Locate every blood parasite and identify its species.
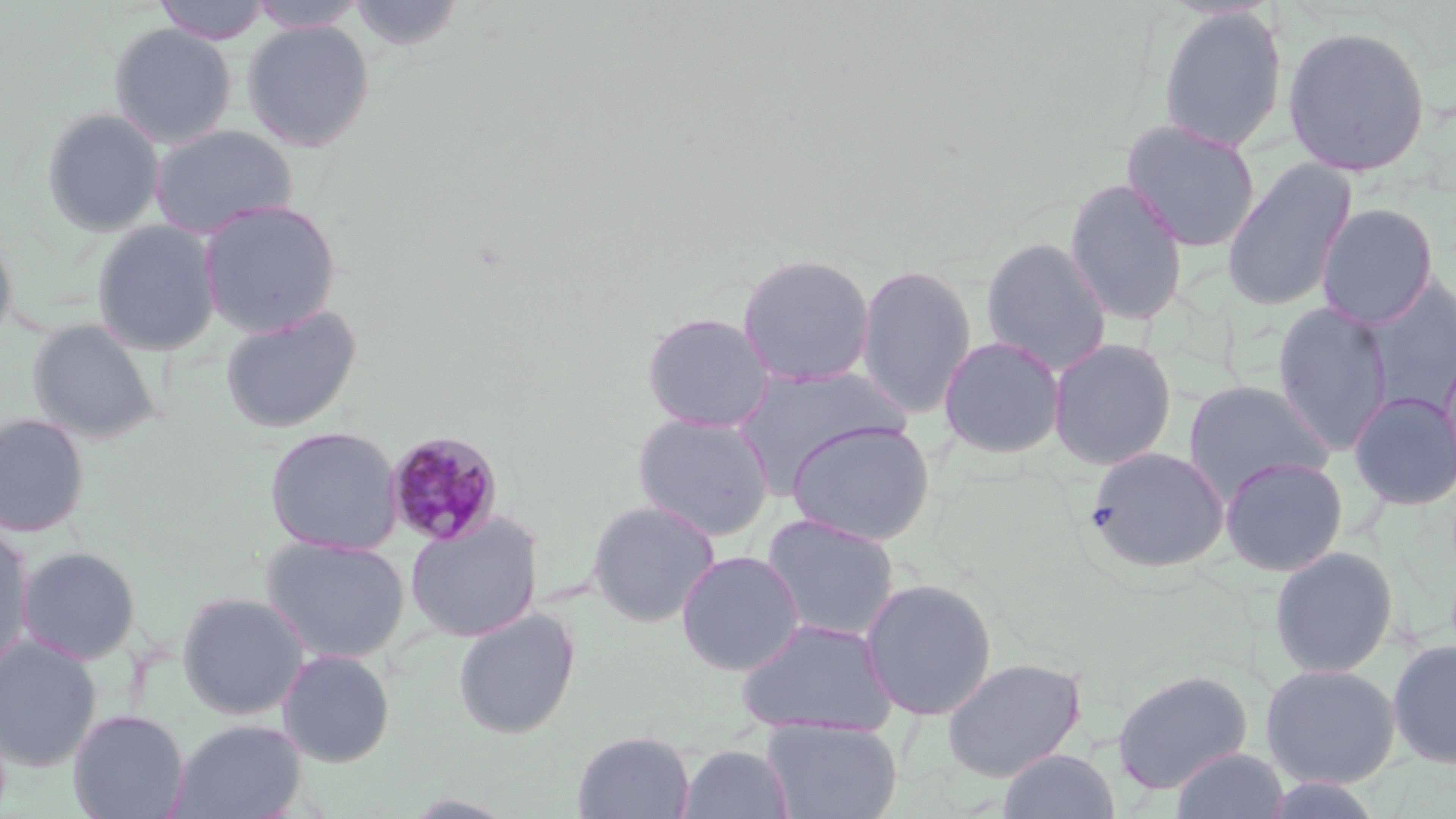
Approximate bounding boxes as named x1/y1/x2/y2 corners in pixels.
Plasmodium malariae-infected red blood cells: (x1=384, y1=431, x2=504, y2=546).
No Plasmodium falciparum, Plasmodium ovale, Plasmodium vivax, Babesia divergens, or Trypanosoma brucei observed.

Uninfected red blood cell locations: (x1=154, y1=0, x2=272, y2=43), (x1=246, y1=0, x2=368, y2=33), (x1=346, y1=0, x2=467, y2=52), (x1=1157, y1=5, x2=1289, y2=154), (x1=242, y1=19, x2=376, y2=152), (x1=108, y1=23, x2=237, y2=148), (x1=1281, y1=24, x2=1432, y2=178), (x1=41, y1=107, x2=164, y2=236), (x1=1121, y1=119, x2=1261, y2=252), (x1=150, y1=124, x2=299, y2=238), (x1=1221, y1=158, x2=1357, y2=313), (x1=1063, y1=177, x2=1189, y2=326), (x1=198, y1=199, x2=342, y2=338), (x1=1316, y1=203, x2=1439, y2=329), (x1=91, y1=220, x2=222, y2=356), (x1=0, y1=228, x2=17, y2=347), (x1=980, y1=237, x2=1112, y2=374), (x1=736, y1=252, x2=876, y2=387), (x1=855, y1=263, x2=977, y2=418), (x1=1360, y1=274, x2=1456, y2=417), (x1=1271, y1=301, x2=1393, y2=455), (x1=219, y1=303, x2=362, y2=435), (x1=641, y1=311, x2=776, y2=433), (x1=26, y1=318, x2=163, y2=444), (x1=938, y1=336, x2=1066, y2=458), (x1=1047, y1=337, x2=1178, y2=470), (x1=1437, y1=344, x2=1456, y2=497), (x1=729, y1=366, x2=910, y2=494), (x1=1182, y1=380, x2=1334, y2=500), (x1=1349, y1=390, x2=1456, y2=511), (x1=633, y1=412, x2=775, y2=542), (x1=0, y1=413, x2=90, y2=537), (x1=786, y1=419, x2=935, y2=546), (x1=263, y1=426, x2=404, y2=555), (x1=1085, y1=447, x2=1230, y2=574), (x1=1219, y1=456, x2=1348, y2=576), (x1=586, y1=499, x2=721, y2=628), (x1=404, y1=513, x2=544, y2=642), (x1=761, y1=513, x2=900, y2=642), (x1=0, y1=522, x2=34, y2=673), (x1=261, y1=536, x2=410, y2=664), (x1=16, y1=546, x2=141, y2=665), (x1=1269, y1=546, x2=1399, y2=678), (x1=675, y1=549, x2=805, y2=676), (x1=859, y1=578, x2=998, y2=720), (x1=177, y1=591, x2=310, y2=720), (x1=452, y1=608, x2=581, y2=739), (x1=735, y1=617, x2=897, y2=736), (x1=0, y1=635, x2=102, y2=772), (x1=1387, y1=639, x2=1456, y2=769), (x1=278, y1=649, x2=395, y2=767), (x1=941, y1=657, x2=1086, y2=781), (x1=1259, y1=662, x2=1401, y2=789), (x1=1111, y1=668, x2=1253, y2=795), (x1=67, y1=708, x2=190, y2=819), (x1=171, y1=719, x2=307, y2=819), (x1=762, y1=719, x2=902, y2=819), (x1=572, y1=730, x2=695, y2=818), (x1=678, y1=744, x2=794, y2=819), (x1=997, y1=748, x2=1121, y2=819), (x1=1170, y1=748, x2=1290, y2=819), (x1=1258, y1=774, x2=1385, y2=818). Slide-level diagnosis: Plasmodium malariae. May-Grünwald-Giemsa-stained preparation. Light microscopy. Captured at 1000x magnification. Thin blood smear. Single field of view. Image is 1456×819 pixels.